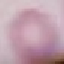
result: no malaria parasites seen
capture: smartphone camera at the microscope eyepiece
preparation: thin blood film
image_type: automatically extracted cell patch, resized to 64 × 64 pixels
stain: Giemsa